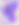

{
  "modality": "micrograph",
  "identification": "Toxoplasma gondii",
  "magnification": "400x"
}